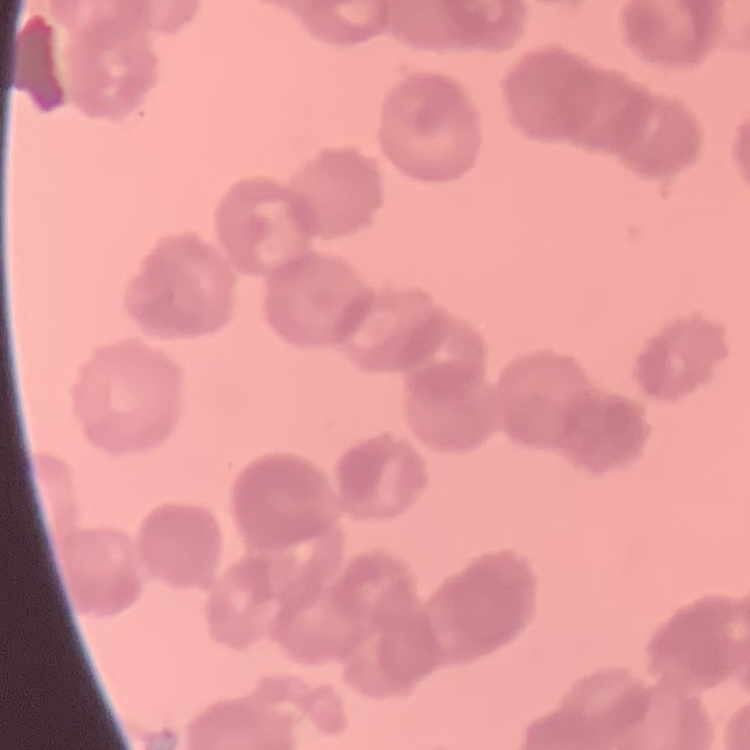

The erythrocytes show rouleaux formation. Thin peripheral smear. Square crop of a larger photomicrograph. Field's or Giemsa stain.